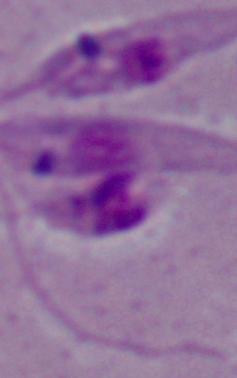

Summary:
  - Modality: micrograph
  - Identification: Leishmania
  - Magnification: 1000x